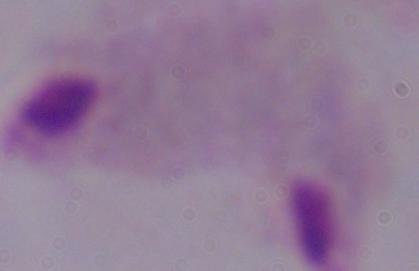

Summary:
  - Magnification: 1000x
  - Identification: trichomonad
  - Modality: micrograph